Classify this cell by malaria status.
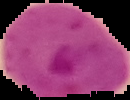
It is parasitized.

Summary:
  - Image type: cell region segmented out of the field of view; surrounding area masked to black
  - Image size: 130×100 pixels
  - Preparation: thin blood film